Assess this cell for malaria.
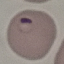

Parasitized.

image type = cell patch, automatically extracted from a larger field of view and resized to 64 × 64 pixels
stain = Giemsa
preparation = thin blood smear
capture = smartphone through the microscope eyepiece